State which parasite is depicted.
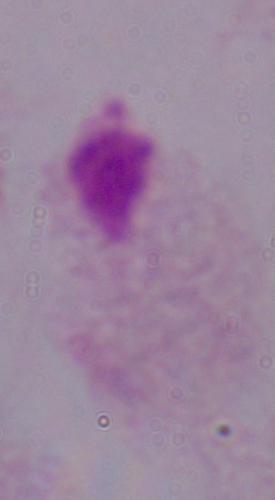
A trichomonad.

Summary:
  - Magnification: 1000x
  - Modality: micrograph